Locate every blood parasite and identify its species.
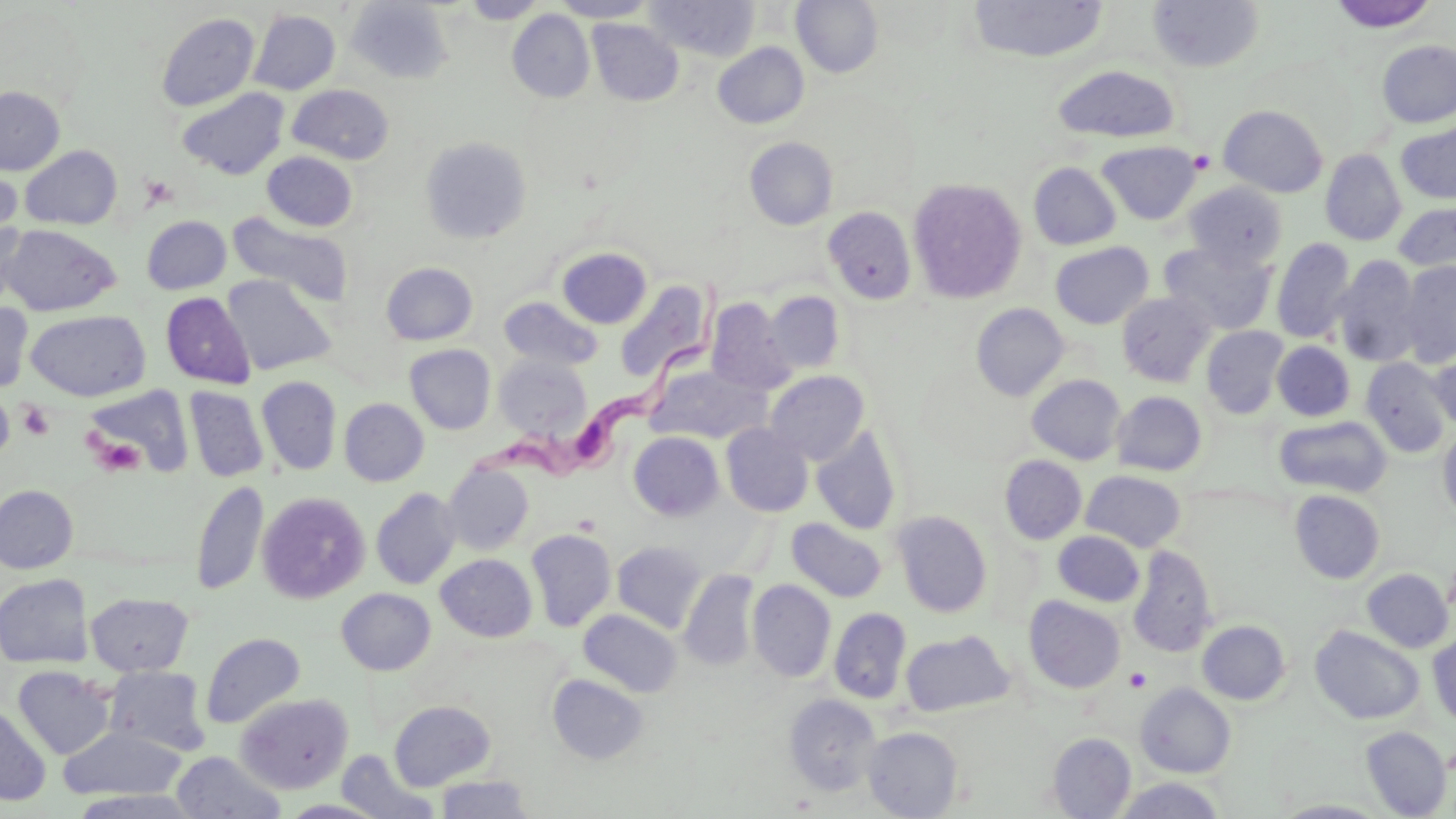
Approximate bounding boxes as named x1/y1/x2/y2 corners in pixels.
Trypanosoma brucei: (x1=469, y1=293, x2=724, y2=489).
No Plasmodium falciparum, Plasmodium ovale, Plasmodium malariae, Plasmodium vivax, or Babesia divergens observed.

Platelet locations: (x1=1189, y1=149, x2=1216, y2=175), (x1=140, y1=174, x2=178, y2=209), (x1=16, y1=402, x2=55, y2=440), (x1=91, y1=434, x2=145, y2=476), (x1=1125, y1=668, x2=1150, y2=691). Uninfected red blood cell locations: (x1=461, y1=0, x2=547, y2=23), (x1=550, y1=0, x2=659, y2=22), (x1=645, y1=0, x2=761, y2=61), (x1=791, y1=0, x2=884, y2=77), (x1=1147, y1=0, x2=1264, y2=73), (x1=345, y1=1, x2=453, y2=83), (x1=966, y1=1, x2=1108, y2=63), (x1=1327, y1=1, x2=1439, y2=33), (x1=507, y1=9, x2=595, y2=103), (x1=249, y1=10, x2=341, y2=95), (x1=156, y1=12, x2=260, y2=112), (x1=587, y1=19, x2=684, y2=105), (x1=1376, y1=40, x2=1456, y2=128), (x1=713, y1=42, x2=809, y2=128), (x1=1053, y1=65, x2=1180, y2=144), (x1=288, y1=85, x2=395, y2=164), (x1=0, y1=86, x2=65, y2=175), (x1=177, y1=87, x2=289, y2=179), (x1=1218, y1=105, x2=1328, y2=197), (x1=1397, y1=123, x2=1456, y2=204), (x1=420, y1=135, x2=532, y2=244), (x1=745, y1=137, x2=838, y2=230), (x1=1097, y1=141, x2=1201, y2=225), (x1=20, y1=145, x2=123, y2=230), (x1=1321, y1=149, x2=1407, y2=246), (x1=261, y1=151, x2=358, y2=231), (x1=1, y1=159, x2=21, y2=254), (x1=1029, y1=162, x2=1121, y2=250), (x1=907, y1=177, x2=1028, y2=303), (x1=1184, y1=183, x2=1288, y2=269), (x1=1394, y1=203, x2=1456, y2=273), (x1=823, y1=206, x2=917, y2=305), (x1=227, y1=211, x2=354, y2=307), (x1=142, y1=215, x2=231, y2=294), (x1=0, y1=218, x2=29, y2=314), (x1=1, y1=224, x2=121, y2=316), (x1=1271, y1=237, x2=1356, y2=344), (x1=1050, y1=242, x2=1153, y2=329), (x1=1159, y1=242, x2=1276, y2=335), (x1=557, y1=247, x2=652, y2=328), (x1=1332, y1=255, x2=1424, y2=368), (x1=381, y1=262, x2=478, y2=345), (x1=1398, y1=262, x2=1456, y2=367), (x1=222, y1=275, x2=334, y2=376), (x1=615, y1=280, x2=714, y2=382), (x1=764, y1=291, x2=845, y2=374), (x1=161, y1=292, x2=254, y2=389), (x1=1116, y1=292, x2=1216, y2=387), (x1=499, y1=296, x2=603, y2=371), (x1=705, y1=299, x2=795, y2=394), (x1=0, y1=302, x2=33, y2=394), (x1=971, y1=303, x2=1069, y2=401), (x1=26, y1=310, x2=150, y2=401), (x1=1201, y1=326, x2=1289, y2=418), (x1=1272, y1=341, x2=1355, y2=421), (x1=404, y1=344, x2=496, y2=434), (x1=1429, y1=347, x2=1456, y2=433), (x1=494, y1=354, x2=592, y2=440), (x1=1361, y1=357, x2=1452, y2=457), (x1=646, y1=364, x2=769, y2=444), (x1=765, y1=371, x2=869, y2=465), (x1=1027, y1=374, x2=1126, y2=465), (x1=256, y1=376, x2=342, y2=475), (x1=83, y1=386, x2=193, y2=477), (x1=184, y1=387, x2=268, y2=482), (x1=0, y1=391, x2=15, y2=462), (x1=1111, y1=391, x2=1207, y2=476), (x1=339, y1=398, x2=429, y2=486), (x1=1274, y1=416, x2=1392, y2=498), (x1=721, y1=423, x2=814, y2=517), (x1=811, y1=425, x2=902, y2=535), (x1=1438, y1=427, x2=1456, y2=524), (x1=629, y1=431, x2=724, y2=521), (x1=999, y1=455, x2=1086, y2=544), (x1=442, y1=463, x2=534, y2=555), (x1=1081, y1=470, x2=1186, y2=552), (x1=191, y1=480, x2=268, y2=596), (x1=1, y1=485, x2=78, y2=574), (x1=371, y1=487, x2=462, y2=589), (x1=1290, y1=490, x2=1385, y2=583), (x1=257, y1=491, x2=370, y2=604), (x1=891, y1=510, x2=992, y2=618), (x1=786, y1=518, x2=888, y2=602), (x1=526, y1=529, x2=616, y2=632), (x1=1053, y1=531, x2=1145, y2=606), (x1=612, y1=540, x2=708, y2=632), (x1=1128, y1=545, x2=1218, y2=657), (x1=436, y1=553, x2=537, y2=642), (x1=1363, y1=568, x2=1453, y2=653), (x1=679, y1=569, x2=759, y2=670), (x1=1, y1=574, x2=92, y2=669), (x1=747, y1=579, x2=836, y2=682), (x1=336, y1=588, x2=436, y2=675), (x1=86, y1=592, x2=193, y2=676), (x1=1024, y1=596, x2=1126, y2=693), (x1=829, y1=607, x2=911, y2=703), (x1=578, y1=609, x2=682, y2=697), (x1=1197, y1=620, x2=1290, y2=704), (x1=1310, y1=625, x2=1425, y2=724), (x1=901, y1=629, x2=1015, y2=717), (x1=201, y1=632, x2=305, y2=729), (x1=1428, y1=633, x2=1456, y2=727), (x1=13, y1=666, x2=116, y2=759), (x1=104, y1=666, x2=212, y2=756), (x1=548, y1=674, x2=649, y2=764), (x1=1136, y1=683, x2=1235, y2=778), (x1=235, y1=692, x2=354, y2=794), (x1=783, y1=694, x2=882, y2=795), (x1=389, y1=700, x2=495, y2=789), (x1=0, y1=702, x2=51, y2=806), (x1=58, y1=725, x2=186, y2=802), (x1=1360, y1=726, x2=1452, y2=818), (x1=863, y1=727, x2=963, y2=818), (x1=1047, y1=733, x2=1136, y2=818), (x1=337, y1=749, x2=437, y2=818), (x1=171, y1=751, x2=285, y2=818), (x1=434, y1=774, x2=534, y2=818), (x1=1115, y1=776, x2=1225, y2=818). Slide-level diagnosis: Trypanosoma brucei. May-Grünwald-Giemsa stain. Optical microscopy. Thin blood smear. Single field of view. Image is 1456×819 pixels. 1000x magnification.